Find each white blood cell.
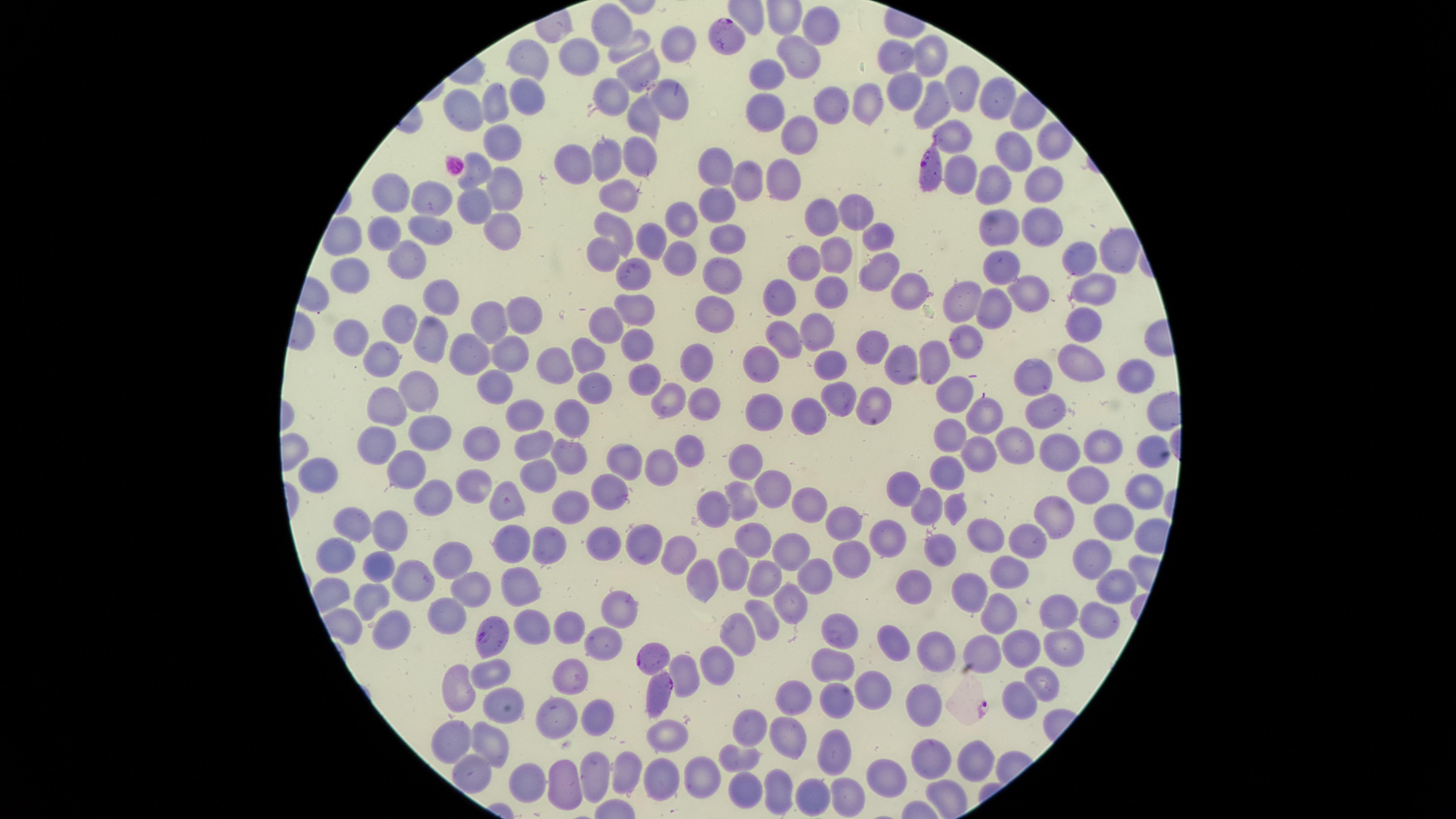
No white blood cells identified.

Approximate marker points as (x, y) in pixels. Uninfected red blood cells: (815, 28), (606, 30), (630, 43), (677, 44), (803, 52), (576, 56), (899, 56), (928, 56), (528, 63), (637, 68), (768, 72), (954, 80), (911, 87), (616, 90), (993, 94), (528, 96), (671, 100), (867, 101), (934, 102), (498, 104), (765, 107), (826, 107), (466, 112), (642, 115), (954, 127), (1051, 132), (798, 138), (498, 146), (1014, 150), (640, 151), (615, 159), (573, 164), (711, 166), (479, 168), (964, 169), (778, 180), (741, 182), (1043, 184), (506, 186), (990, 186), (393, 194), (627, 194), (433, 200), (476, 203), (717, 208), (852, 213), (676, 219), (504, 221), (1042, 221), (823, 224), (429, 228), (611, 228), (389, 230), (996, 231), (878, 235), (649, 242), (726, 245), (839, 251), (1113, 252), (605, 256), (1073, 257), (410, 261), (680, 262), (805, 263), (871, 268), (1000, 268), (359, 272), (722, 275), (637, 284), (1096, 290), (1026, 292), (783, 293), (913, 294), (445, 297), (821, 297), (962, 306), (521, 310), (638, 310), (993, 310), (707, 315), (487, 317), (611, 319), (403, 322), (1079, 326), (813, 332), (429, 333), (782, 334), (356, 336), (963, 339), (636, 346), (457, 349), (506, 352), (589, 354), (866, 354), (381, 359), (932, 361), (898, 362), (689, 363), (759, 364), (558, 366), (829, 366), (1080, 366), (1136, 374), (644, 378), (1041, 381), (597, 386), (487, 391), (417, 393), (951, 395), (844, 396), (670, 400), (706, 406), (763, 406), (384, 407), (871, 409), (523, 410), (1043, 411), (567, 413), (815, 414), (984, 417), (430, 427), (954, 434), (482, 437), (381, 439), (1098, 439), (1017, 444), (1143, 446), (1064, 447), (534, 448), (689, 450), (981, 454), (627, 458), (748, 465), (661, 468), (946, 474), (404, 477), (539, 478), (322, 480), (1087, 480), (469, 486), (773, 487), (906, 487), (608, 492), (742, 497), (1140, 497), (813, 501), (432, 502), (567, 502), (929, 503), (958, 503), (515, 508), (714, 508), (1055, 511), (849, 513), (351, 519), (1114, 521), (980, 532), (390, 535), (750, 537), (642, 540), (547, 542), (1021, 542), (940, 543), (888, 544), (604, 547), (515, 549), (786, 552), (852, 556), (1090, 556), (673, 557), (341, 562), (377, 562), (449, 563), (734, 564), (1008, 572), (813, 574), (768, 577), (700, 582), (970, 583), (421, 587), (468, 587), (522, 588), (1112, 589), (340, 592), (913, 592), (367, 597), (794, 597), (1001, 608), (1058, 608), (448, 611), (620, 612), (1092, 615), (762, 616), (394, 626), (569, 626), (836, 630), (533, 631), (739, 631), (604, 639), (890, 646), (1065, 646), (1023, 647), (931, 651), (984, 651), (715, 665), (831, 665), (570, 667), (486, 670), (685, 670), (1043, 678), (875, 690), (453, 692), (929, 696), (799, 697), (1019, 700), (835, 702), (498, 707), (557, 714), (597, 715), (753, 725), (669, 734), (788, 739), (451, 744), (487, 749), (979, 753), (836, 754), (741, 758), (932, 761), (622, 769), (590, 771), (888, 771), (708, 774), (469, 776), (529, 782), (567, 782), (659, 782), (745, 792), (782, 792), (842, 797), (813, 803). Parasitized red blood cells: (728, 35), (934, 175), (490, 633), (653, 657), (662, 691). Species: Plasmodium falciparum. Photographed with a smartphone camera through the microscope eyepiece. One field of view of the specimen. Presence: malaria parasites identified. Circular visible region. Giemsa stain. Thin blood smear. Image is 1456×819 pixels.